Report the malaria status of this cell.
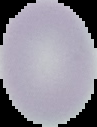
It is uninfected.

Cell region segmented out of the field of view; the surrounding area is masked to black. Image is 97×127 pixels. From a thin blood smear.